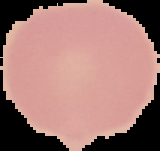

Malaria status: uninfected. Segmented cell region on a black background. Image is 160×151 pixels. From a thin blood smear.